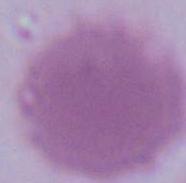
Summary:
  - Modality: photomicrograph
  - Identification: red blood cell
  - Magnification: 1000x